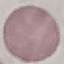

Result: negative for malaria parasites. Giemsa-stained preparation. Thin smear of blood. Photographed with a smartphone camera at the microscope eyepiece. Automatically extracted cell patch, resized to 64 × 64 pixels.